Locate and identify every blood parasite.
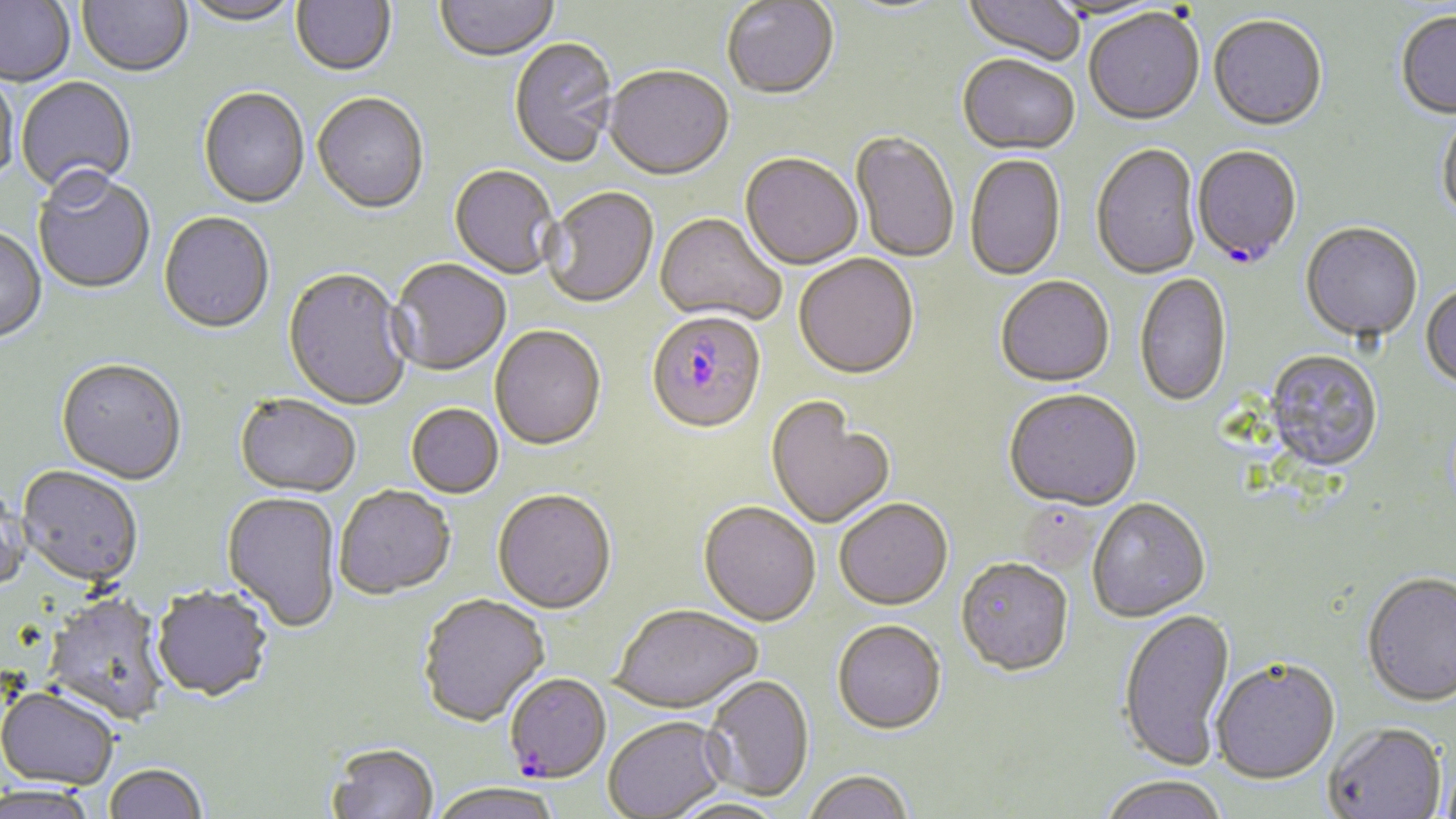

Approximate bounding boxes as [x1, y1, x2, y2] in pixels.
Plasmodium falciparum-infected red blood cells: [1192, 147, 1302, 268], [646, 313, 767, 437], [504, 674, 611, 785].
No Plasmodium ovale, Plasmodium malariae, Plasmodium vivax, Babesia divergens, or Trypanosoma brucei observed.

Summary:
  - Uninfected red blood cell locations: [0, 0, 76, 88], [76, 0, 194, 79], [180, 0, 302, 28], [291, 0, 396, 78], [435, 0, 560, 64], [963, 0, 1084, 66], [1042, 0, 1168, 23], [722, 1, 839, 103], [1083, 10, 1205, 128], [1394, 11, 1456, 120], [1208, 17, 1328, 133], [509, 38, 619, 171], [957, 56, 1080, 157], [603, 68, 734, 184], [0, 71, 19, 188], [16, 77, 137, 199], [199, 89, 309, 210], [312, 94, 429, 216], [1437, 114, 1456, 226], [850, 132, 959, 264], [1092, 145, 1202, 281], [740, 155, 863, 272], [965, 155, 1066, 282], [449, 166, 560, 280], [32, 170, 156, 295], [541, 189, 659, 310], [158, 213, 275, 336], [654, 215, 786, 327], [1300, 224, 1422, 344], [0, 228, 47, 345], [794, 256, 919, 382], [388, 261, 511, 377], [283, 270, 411, 411], [1135, 273, 1232, 409], [996, 277, 1115, 389], [1420, 284, 1456, 392], [490, 326, 606, 452], [1264, 351, 1383, 475], [56, 360, 188, 486], [1004, 391, 1142, 513], [234, 395, 361, 499], [766, 399, 895, 530], [406, 405, 503, 499], [16, 466, 144, 587], [0, 484, 31, 595], [334, 487, 456, 601], [492, 491, 617, 617], [221, 492, 341, 633], [1088, 500, 1211, 624], [834, 501, 953, 613], [698, 503, 821, 628], [955, 561, 1074, 680], [1362, 574, 1456, 710], [151, 586, 273, 703], [42, 590, 171, 725], [418, 595, 551, 729], [611, 606, 762, 716], [1117, 609, 1236, 774], [832, 622, 947, 737], [1211, 661, 1340, 788], [702, 675, 814, 803], [0, 686, 119, 790], [604, 718, 729, 818], [1324, 724, 1447, 819], [327, 744, 439, 819], [103, 763, 208, 819], [803, 773, 914, 819], [1098, 778, 1228, 819], [430, 783, 563, 819], [0, 784, 100, 818], [665, 798, 792, 818]
  - Slide-level diagnosis: Plasmodium falciparum
  - Preparation: thin blood smear
  - Image size: 1456×819 pixels
  - Modality: light microscopy
  - Magnification: 1000x
  - Stain: May-Grünwald-Giemsa
  - Field of view: single